Look for Plasmodium parasites.
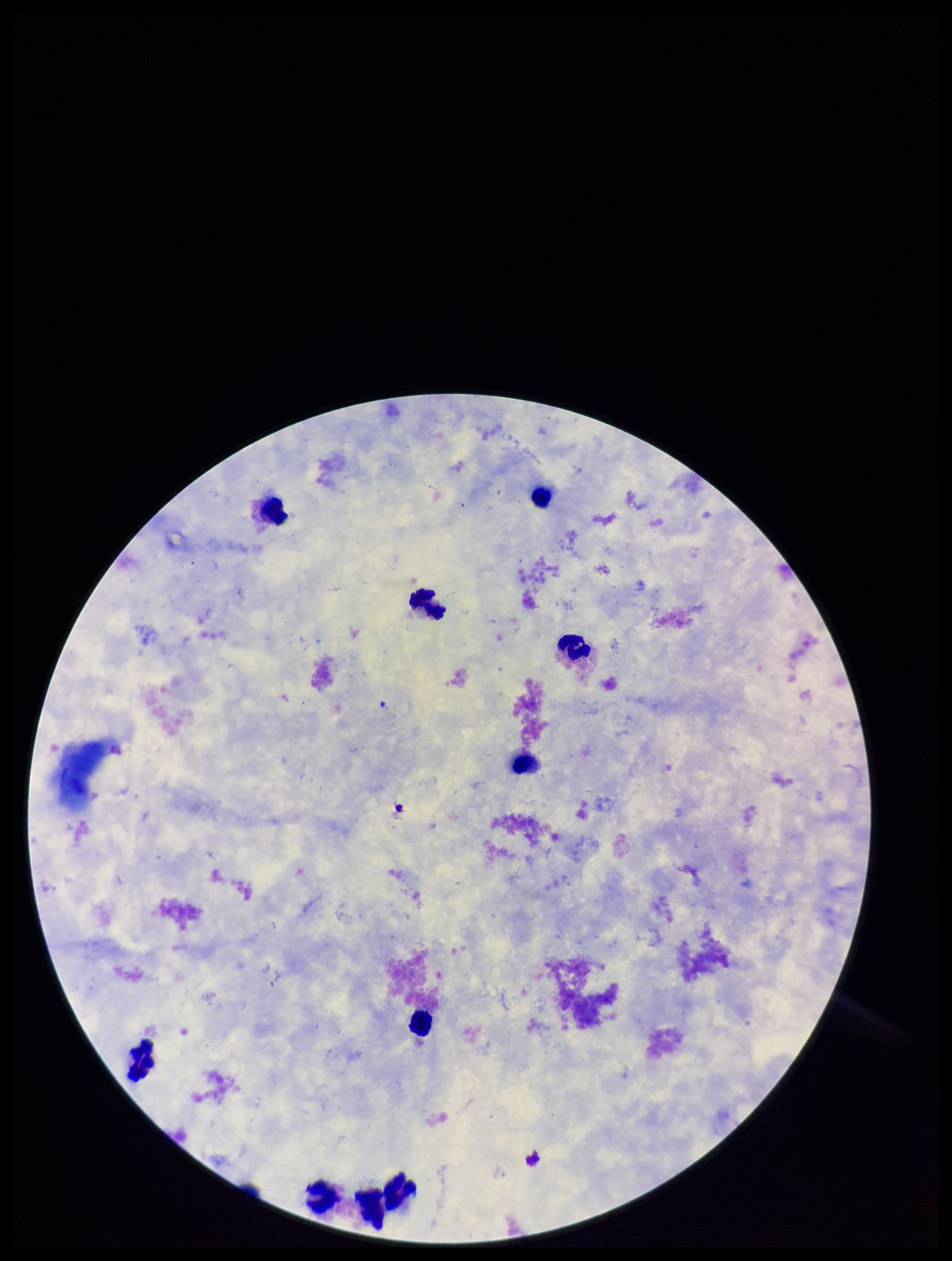

None detected.

Summary:
  - Capture: smartphone photograph through the microscope eyepiece
  - Parasite count: 0
  - Image size: 952×1261 pixels
  - Stain: Giemsa
  - Leukocyte count: 10
  - Patient malaria status: negative
  - Field of view: one from this slide
  - Preparation: thick